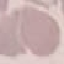 Malaria status: uninfected. Photographed with a smartphone camera at the microscope eyepiece. Giemsa-stained preparation. Cell patch, automatically extracted from a larger field of view and resized to 64 × 64 pixels. Thin blood smear.